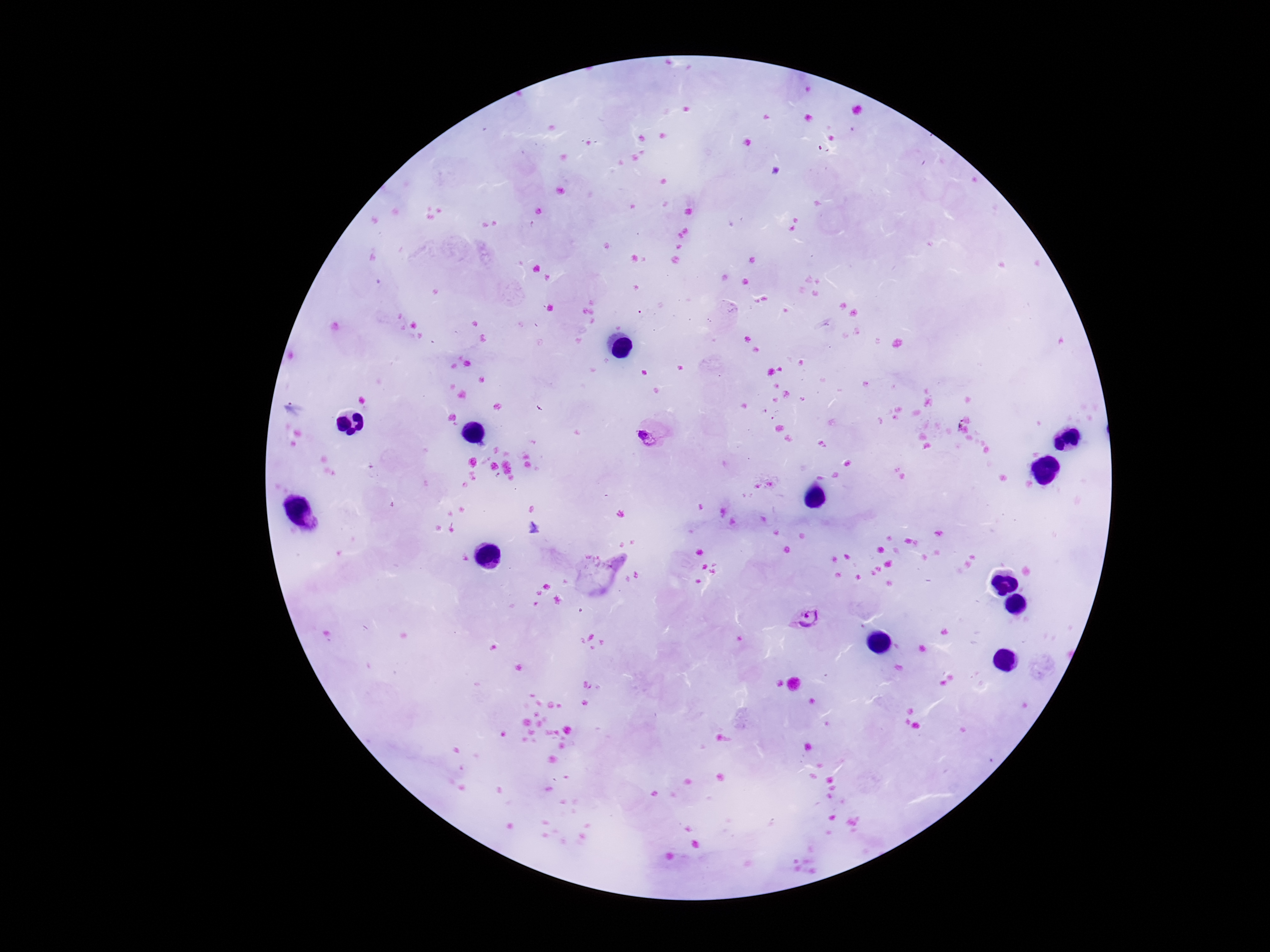
Approximate centers as {x, y} in pixels.
Summary:
  - Plasmodium parasite locations: {295, 408}, {961, 422}, {647, 439}, {808, 619}
  - Magnification: 100x
  - Field of view: one from this slide
  - Patient malaria status: infected
  - Image size: 1270×952 pixels
  - Preparation: thick blood film
  - Stain: Giemsa
  - Capture: smartphone camera through the microscope eyepiece